Give the position of every Plasmodium parasite.
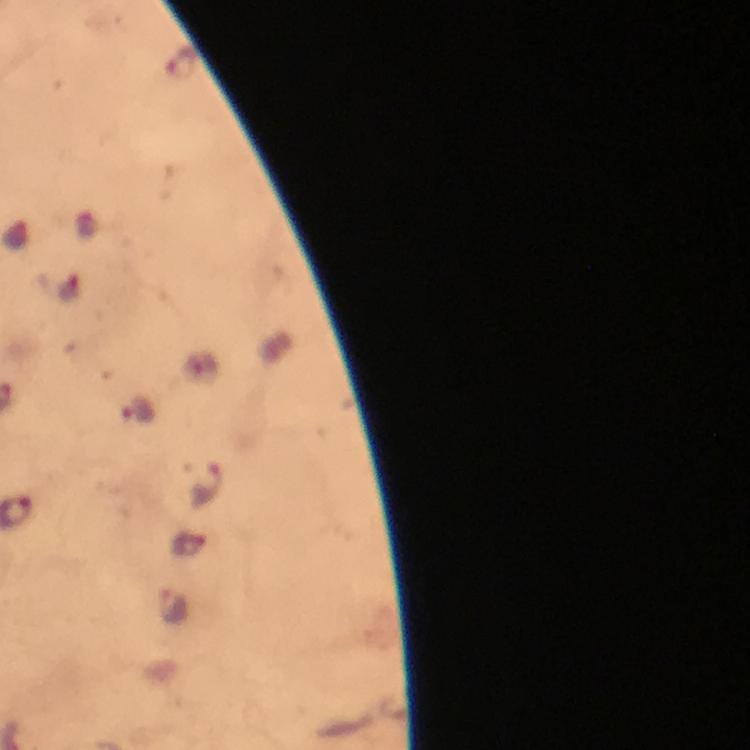

Approximate centers as (x, y) in pixels.
Plasmodium parasites: (184, 65), (136, 410), (206, 482), (189, 545).

Cropped region of a single field of view. Giemsa stain. Immersion oil was used. From a diagnostic examination for malaria. Image is 750×750 pixels. Thick blood smear. 100x magnification. Photographed with a smartphone mounted on the microscope.